Describe the morphology of the erythrocytes.
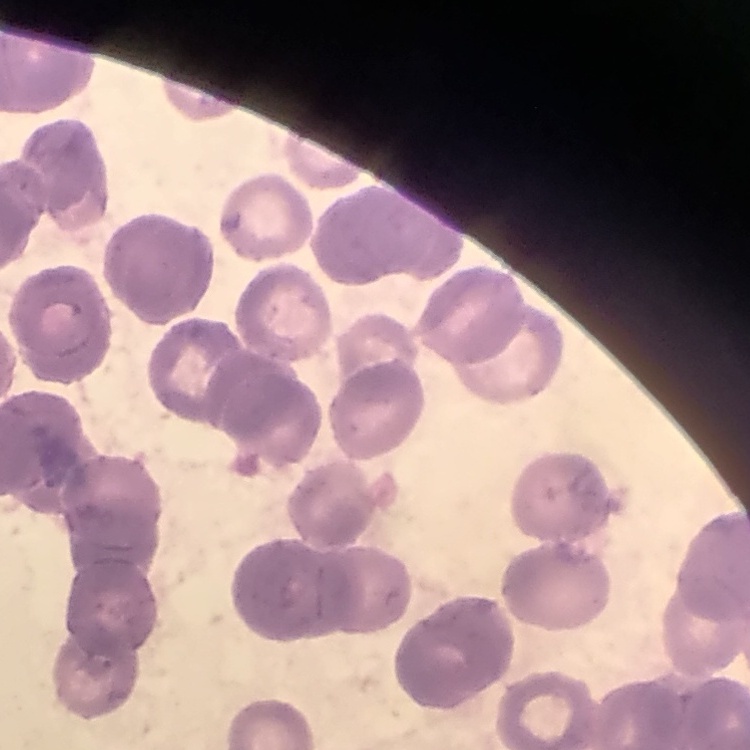

Rouleaux formation.

Summary:
  - Stain: Field's or Giemsa
  - Image type: one tile cut from a larger photomicrograph
  - Preparation: thin peripheral smear